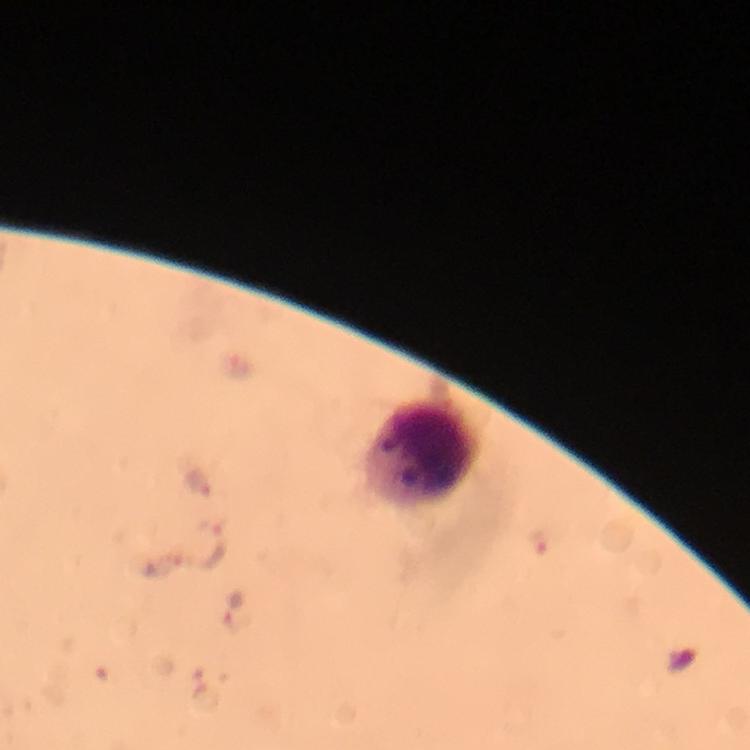
Approximate centers as (x, y) in pixels.
Summary:
  - Leukocyte locations: (424, 451)
  - Plasmodium parasite locations: (199, 483), (538, 541), (214, 546), (231, 609)
  - Stain: Giemsa
  - Preparation: thick blood film
  - Magnification: 100x
  - Capture: smartphone mounted on the microscope
  - Context: from a diagnostic examination for malaria
  - Cropped from: a single field of view
  - Immersion oil: used
  - Image size: 750×750 pixels